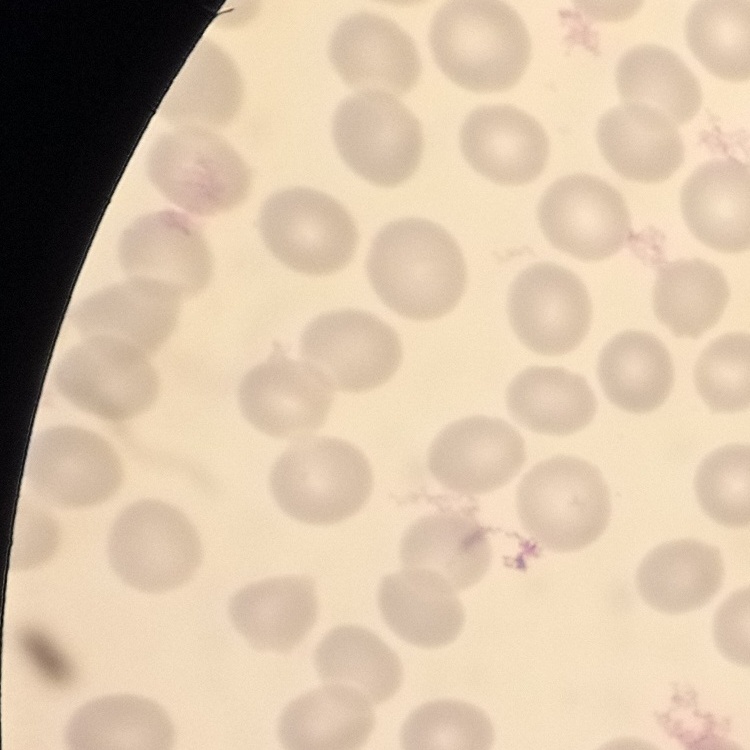

The erythrocytes show no rouleaux formation. Stained with either Field's or Giemsa. Thin blood smear. Square crop of a larger photomicrograph.